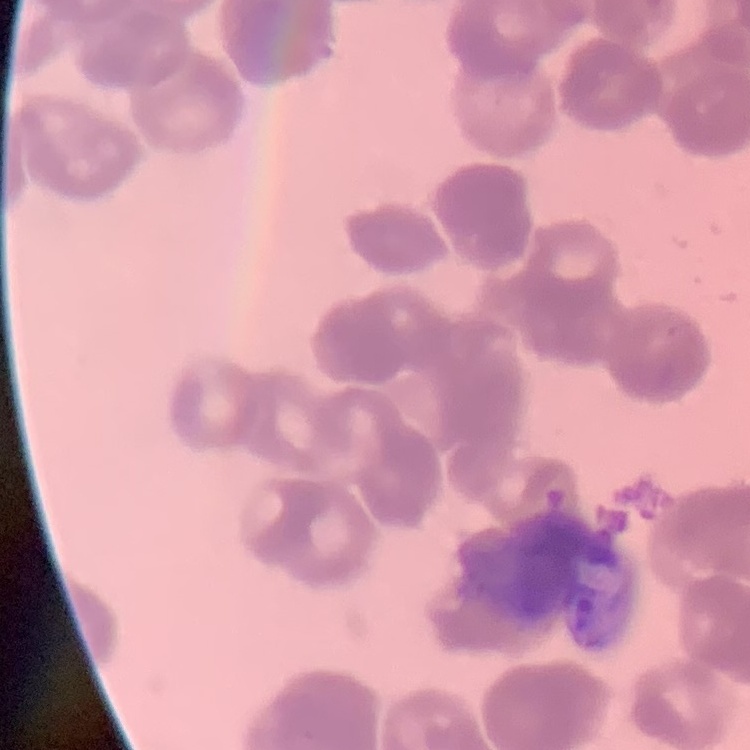
{
  "erythrocyte_morphology": "rouleaux formation",
  "stain": "Field's or Giemsa",
  "image_type": "square crop of a larger photomicrograph",
  "preparation": "thin blood smear"
}